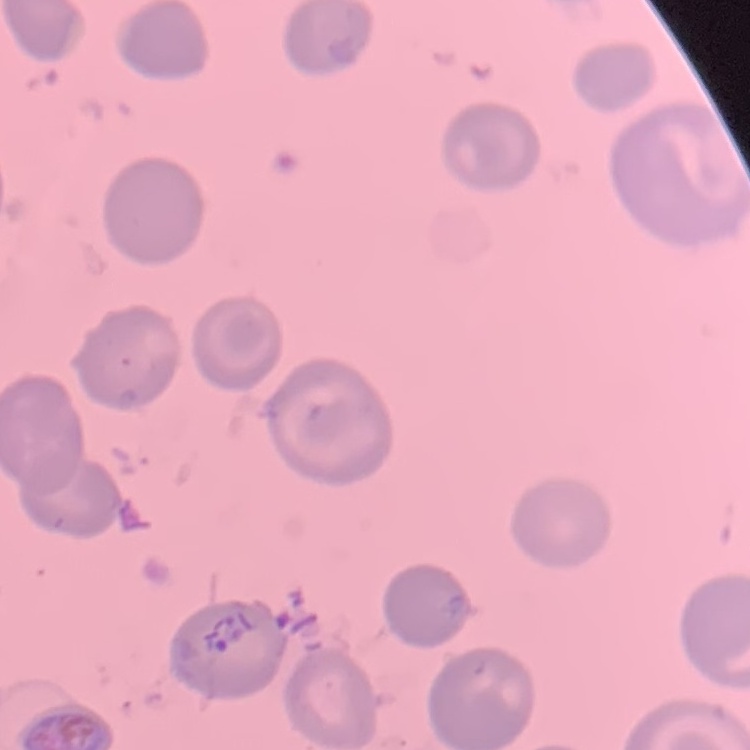
{
  "erythrocyte_morphology": "no rouleaux formation",
  "stain": "Field's or Giemsa",
  "preparation": "thin blood smear",
  "image_type": "square crop of a larger photomicrograph"
}